Classify this cell by malaria status.
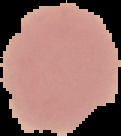

It is uninfected.

Summary:
  - Preparation: thin blood film
  - Image size: 121×136 pixels
  - Image type: segmented cell region on a black background